Report the malaria status of this cell.
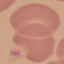

It is uninfected.

Thin blood smear. Automatically extracted cell patch, resized to 64 × 64 pixels. Giemsa stain. Photographed with a smartphone camera at the microscope eyepiece.